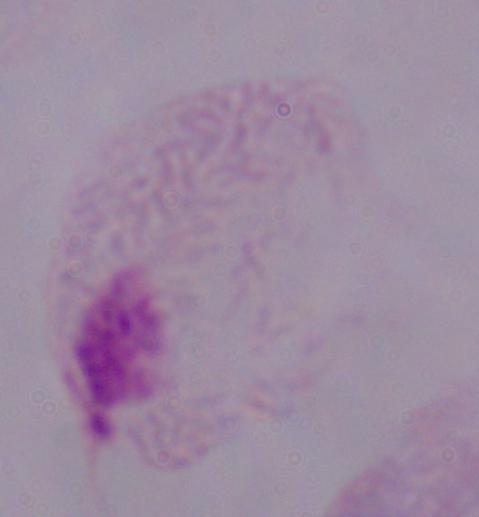
A trichomonad is seen. Captured at 1000x magnification. Micrograph.